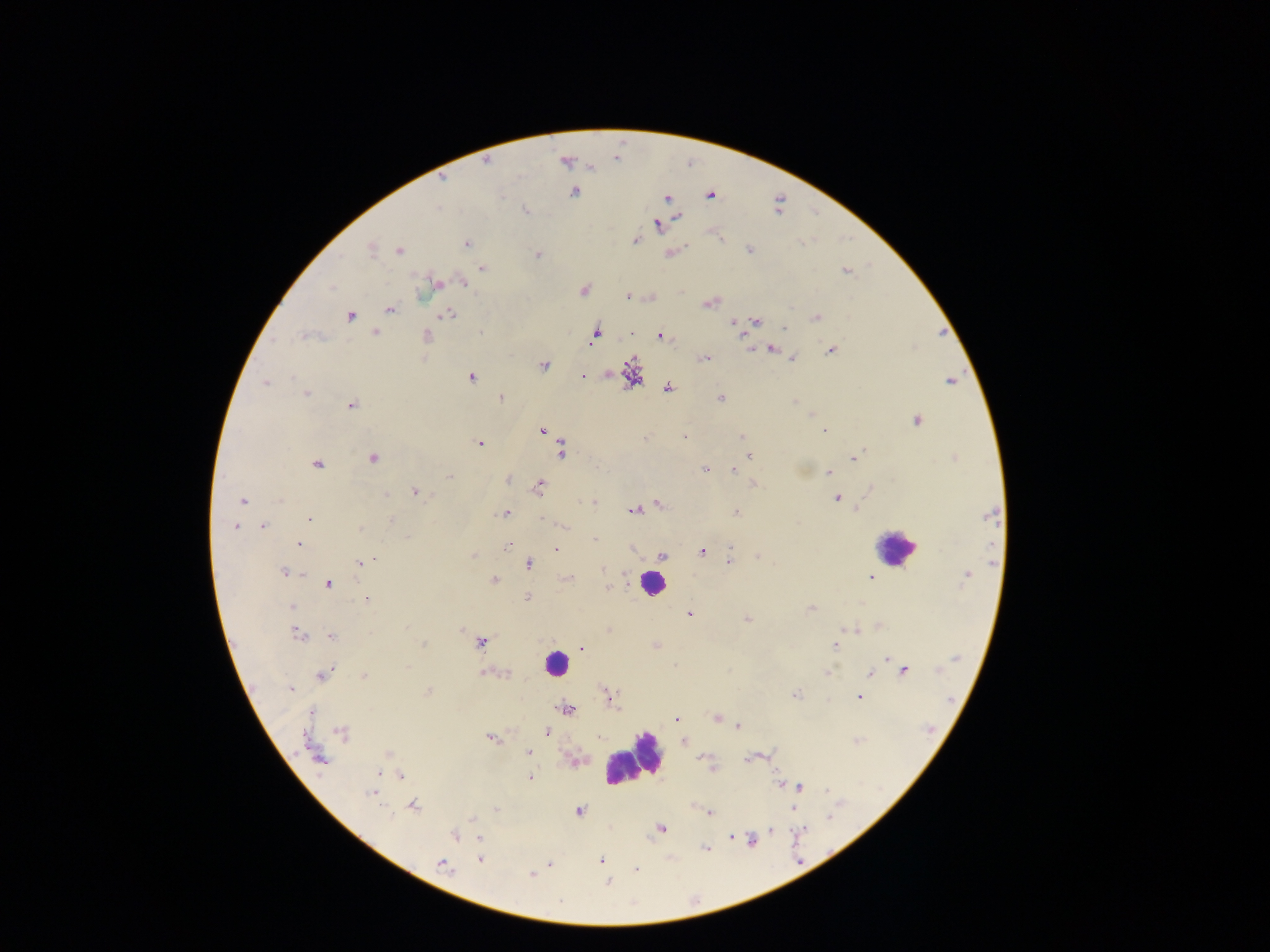

Approximate centers as [x, y] in pixels.
Summary:
  - Malaria parasite locations: [486, 160], [566, 161], [442, 179], [574, 191], [710, 194], [666, 198], [678, 217], [658, 224], [635, 240], [466, 243], [370, 249], [749, 249], [398, 251], [670, 252], [536, 256], [482, 267], [846, 270], [463, 282], [437, 283], [583, 290], [629, 296], [650, 297], [710, 303], [390, 309], [445, 314], [350, 316], [816, 317], [734, 321], [757, 321], [785, 330], [375, 332], [595, 334], [629, 334], [660, 335], [306, 336], [425, 336], [771, 348], [749, 349], [830, 350], [704, 358], [792, 358], [543, 365], [632, 375], [470, 376], [582, 376], [949, 381], [265, 383], [667, 388], [305, 393], [500, 398], [720, 398], [351, 404], [916, 420], [542, 430], [824, 432], [684, 437], [742, 437], [646, 438], [480, 444], [561, 449], [750, 456], [372, 458], [853, 458], [317, 464], [704, 469], [734, 470], [827, 472], [449, 476], [508, 479], [753, 484], [538, 486], [871, 488], [416, 492], [836, 498], [242, 501], [592, 502], [657, 503], [634, 510], [505, 513], [735, 513], [990, 514], [544, 518], [307, 519], [235, 526], [262, 526], [299, 543], [507, 546], [555, 549], [631, 549], [701, 551], [472, 555], [757, 556], [662, 557], [728, 561], [362, 563], [528, 563], [284, 572], [966, 576], [568, 577], [871, 577], [494, 580], [328, 584], [607, 588], [526, 597], [367, 599], [811, 609], [688, 613], [746, 619], [878, 625], [852, 629], [608, 631], [297, 634], [332, 636], [480, 641], [423, 644], [654, 645], [836, 646], [580, 647], [886, 658], [895, 664], [903, 670], [827, 671], [485, 672], [323, 674], [868, 674], [364, 676], [290, 688], [429, 691], [795, 694], [859, 695], [609, 697], [566, 709], [311, 712], [677, 718], [717, 718], [737, 726], [547, 731], [341, 732], [490, 738], [683, 742], [528, 752], [388, 754], [317, 756], [753, 757], [573, 760], [711, 768], [377, 773], [400, 775], [529, 778], [781, 784], [798, 787], [372, 792], [412, 805], [792, 808], [496, 809], [578, 810], [709, 813], [660, 828], [771, 829], [454, 835], [731, 836], [478, 838], [752, 841], [706, 849], [479, 859], [600, 860], [550, 863], [442, 864], [636, 869], [531, 874], [608, 882]
  - Leukocyte locations: [895, 548], [652, 583], [555, 663], [633, 759]
  - Capture: mobile-phone photograph through a microscope
  - Preparation: thick blood smear
  - Country: Ghana
  - Image size: 1270×952 pixels
  - Field of view: single